Outline each uninfected red blood cell.
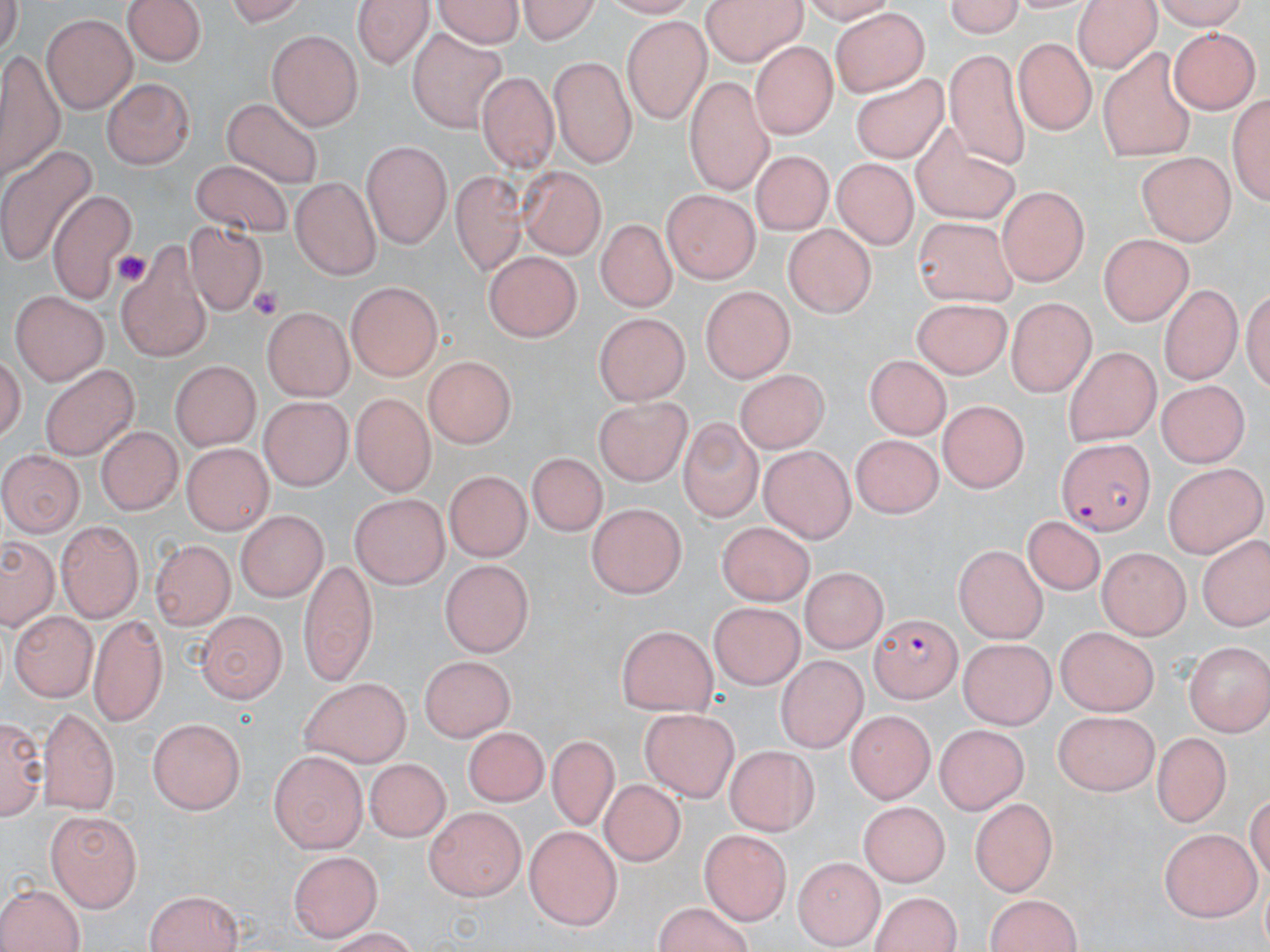
Approximate bounding boxes as (x1,y1)-(x2,y2) corner pairs in pixels.
Uninfected red blood cells: (126,0)-(207,69), (356,0)-(433,67), (430,0)-(527,49), (514,0)-(605,43), (699,0)-(808,63), (939,0)-(1032,35), (217,1)-(313,26), (1074,4)-(1159,75), (829,8)-(928,95), (42,14)-(138,113), (620,17)-(713,122), (403,23)-(514,137), (1167,27)-(1255,115), (266,32)-(365,127), (1012,37)-(1095,138), (750,40)-(838,139), (944,48)-(1037,170), (1,51)-(64,196), (1095,52)-(1201,158), (549,56)-(636,166), (848,65)-(954,170), (476,71)-(560,171), (683,73)-(776,195), (104,76)-(192,169), (218,91)-(332,197), (1229,92)-(1267,208), (909,122)-(1022,226), (360,138)-(449,248), (0,144)-(98,269), (744,149)-(839,241), (1137,153)-(1232,245), (189,163)-(295,235), (834,163)-(915,248), (518,167)-(606,259), (449,171)-(529,267), (291,178)-(379,279), (999,187)-(1088,288), (48,188)-(139,301), (662,190)-(759,286), (914,215)-(1018,308), (597,220)-(673,313), (181,221)-(263,323), (781,226)-(878,316), (1096,235)-(1191,327), (484,251)-(579,345), (115,254)-(216,360), (346,282)-(440,381), (1157,284)-(1243,383), (699,287)-(796,384), (10,289)-(109,384), (909,297)-(1014,378), (1004,299)-(1096,396), (264,307)-(353,404), (594,314)-(686,405), (1062,347)-(1159,446), (421,354)-(516,449), (864,356)-(953,438), (170,358)-(262,447), (735,365)-(828,453), (39,366)-(142,456), (1157,381)-(1247,469), (592,391)-(688,482), (348,395)-(436,495), (938,397)-(1028,491), (258,398)-(352,488), (680,417)-(761,520), (97,427)-(180,516), (850,432)-(939,517), (183,444)-(270,535), (759,446)-(861,541), (0,452)-(82,538), (526,454)-(608,538), (1162,462)-(1264,554), (444,470)-(528,562), (348,494)-(451,585), (586,505)-(684,601), (233,511)-(331,601), (720,519)-(818,603), (1023,520)-(1105,598), (55,521)-(146,622), (1198,530)-(1269,632), (4,538)-(56,627), (148,540)-(234,630), (951,548)-(1048,644), (1094,548)-(1189,640), (297,556)-(380,681), (438,561)-(535,653), (805,566)-(885,655), (705,597)-(809,691), (9,607)-(95,699), (198,612)-(285,702), (86,613)-(169,722), (615,623)-(714,713), (1052,626)-(1155,713), (958,638)-(1058,724), (1184,642)-(1268,735), (777,652)-(862,752), (418,655)-(516,737), (298,676)-(411,769), (41,703)-(119,813), (640,705)-(738,801), (1052,708)-(1157,796), (846,710)-(936,804), (2,713)-(44,820), (148,717)-(246,814), (933,723)-(1024,812), (463,724)-(553,812), (1151,733)-(1234,826), (549,735)-(617,827), (725,746)-(818,836), (268,750)-(367,849), (362,757)-(452,845), (598,776)-(688,870), (968,796)-(1057,896), (858,800)-(952,889), (423,806)-(526,899), (45,811)-(144,911), (525,824)-(625,928), (1156,828)-(1263,918), (701,830)-(791,922), (291,847)-(384,941), (24,850)-(126,948), (795,857)-(882,948), (3,882)-(86,952), (143,889)-(246,952), (870,890)-(959,952), (985,896)-(1081,952), (653,901)-(756,951).

Summary:
  - Plasmodium falciparum-infected red blood cell locations: (1053,436)-(1154,533), (869,613)-(963,702)
  - Platelet locations: (249,285)-(284,324)
  - Slide-level diagnosis: Plasmodium falciparum
  - Field of view: single
  - Modality: light microscopy
  - Image size: 1270×952 pixels
  - Preparation: thin blood film
  - Magnification: 1000x
  - Stain: May-Grünwald-Giemsa